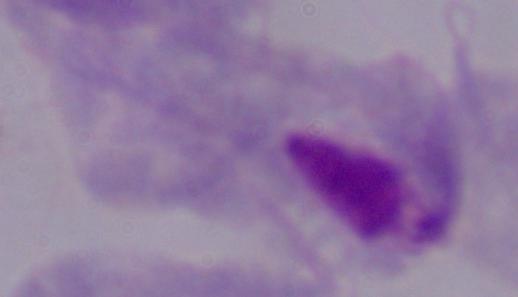 1000x magnification. A trichomonad is shown. Micrograph.